Describe the morphology of the erythrocytes.
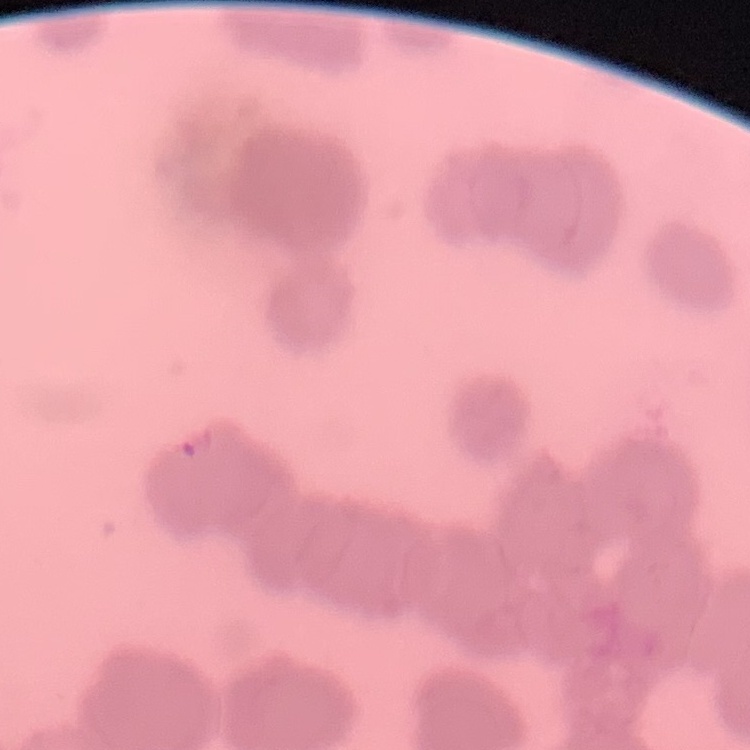

They show rouleaux formation.

preparation = thin blood film
stain = Field's or Giemsa
image type = one tile cut from a larger photomicrograph